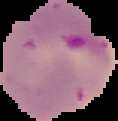

preparation = thin blood smear
image size = 118×121 pixels
image type = cell region segmented out of the field of view; surrounding area masked to black
malaria status = parasitized